Draw a bounding box around every malaria parasite.
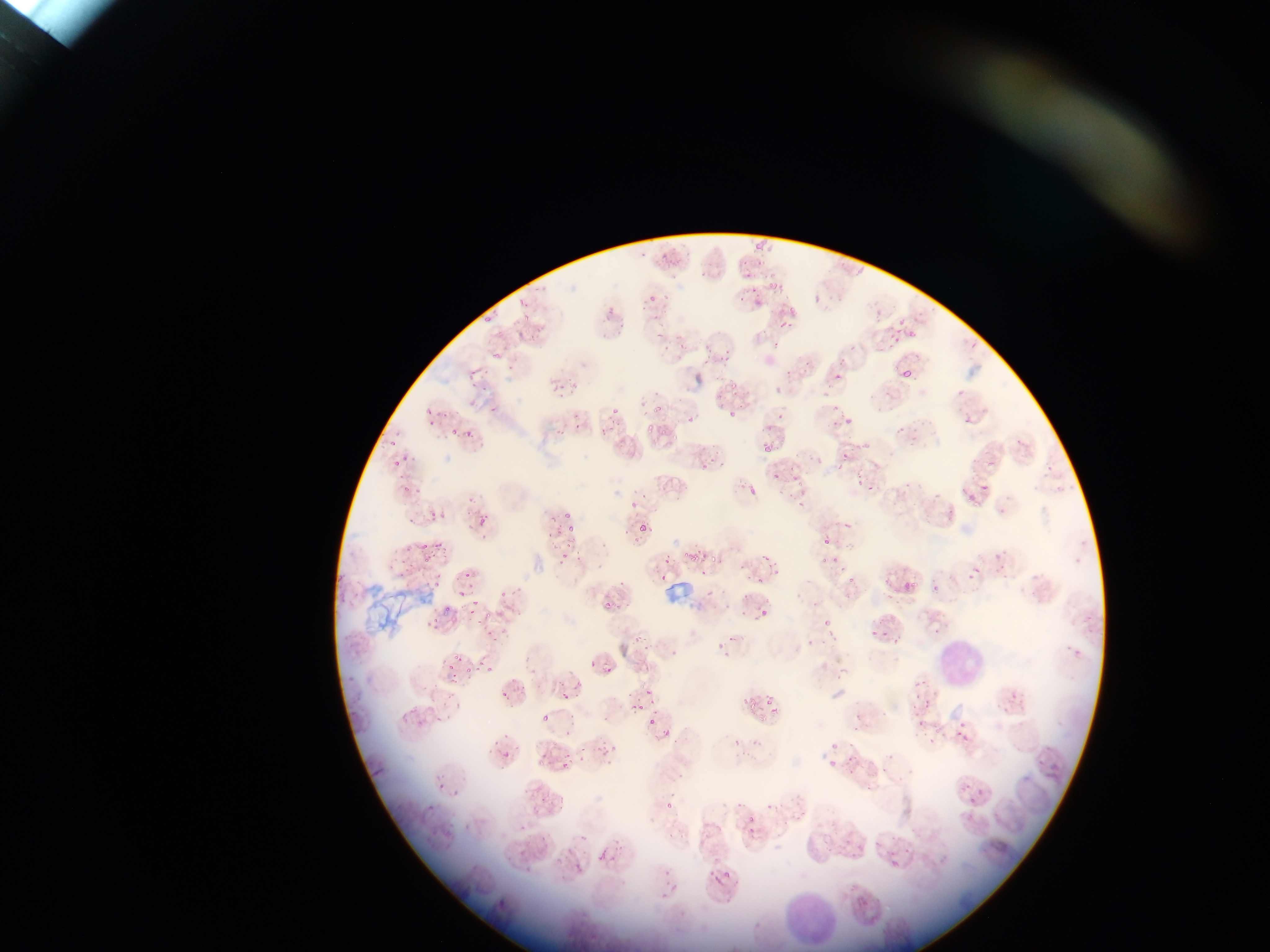
Approximate bounding boxes as (left, top, right, bottom) in pixels.
Malaria parasites: (766, 282, 774, 291), (605, 307, 616, 320), (536, 324, 545, 333), (904, 368, 913, 377), (957, 389, 965, 397), (603, 401, 619, 428), (649, 402, 660, 415), (488, 404, 501, 413), (830, 407, 855, 430), (728, 410, 737, 418), (683, 414, 703, 427), (426, 416, 438, 426), (643, 424, 657, 433), (594, 426, 608, 436), (464, 427, 474, 438), (569, 427, 579, 437), (451, 428, 460, 437), (661, 429, 667, 438), (673, 434, 684, 443), (760, 442, 775, 453), (834, 450, 850, 470), (788, 459, 807, 479), (391, 461, 401, 467), (696, 464, 712, 475), (771, 473, 786, 486), (850, 475, 867, 496), (398, 480, 418, 497), (746, 483, 768, 497), (959, 491, 978, 506), (783, 492, 799, 505), (627, 503, 643, 514), (407, 510, 417, 528), (428, 510, 440, 523), (561, 510, 569, 520), (476, 516, 489, 523), (565, 520, 579, 532), (637, 526, 647, 534), (824, 538, 832, 547), (419, 539, 432, 553), (435, 545, 455, 562), (555, 549, 568, 560), (661, 552, 673, 576), (683, 552, 700, 563), (708, 552, 718, 565), (815, 552, 834, 563), (761, 553, 777, 566), (421, 555, 430, 565), (827, 555, 841, 573), (396, 560, 413, 582), (963, 566, 985, 583), (695, 569, 708, 582), (653, 571, 666, 583), (459, 572, 478, 587), (754, 574, 769, 589), (843, 574, 861, 591), (431, 578, 444, 589), (905, 581, 917, 591), (932, 585, 940, 593), (806, 586, 833, 612), (457, 587, 468, 599), (608, 594, 633, 609), (600, 600, 613, 612), (758, 602, 773, 618), (466, 605, 481, 620), (442, 607, 455, 615), (821, 611, 841, 633), (422, 619, 445, 639), (876, 629, 886, 638), (799, 630, 823, 654), (627, 635, 638, 646), (712, 642, 727, 655), (447, 652, 465, 661), (588, 658, 598, 667), (445, 661, 459, 673), (603, 665, 615, 675), (463, 667, 468, 675), (481, 667, 492, 673), (446, 672, 463, 687), (636, 679, 653, 696), (575, 680, 584, 689), (557, 689, 573, 700), (500, 691, 508, 700), (911, 694, 936, 730), (742, 698, 753, 713), (765, 698, 770, 708), (632, 703, 641, 712), (411, 705, 424, 720), (434, 711, 454, 724), (645, 712, 656, 727), (542, 714, 550, 723), (946, 717, 973, 743), (411, 721, 428, 731), (559, 726, 574, 741), (917, 728, 948, 749), (660, 729, 670, 739), (728, 730, 757, 757), (487, 735, 504, 747), (827, 735, 844, 753), (575, 742, 587, 767), (596, 746, 618, 763), (502, 751, 511, 760), (821, 755, 839, 773), (839, 756, 863, 780), (555, 758, 572, 779), (868, 760, 894, 778), (435, 782, 445, 793), (454, 788, 462, 801), (965, 794, 982, 809), (552, 797, 565, 815), (665, 797, 673, 810), (424, 801, 435, 811), (531, 801, 544, 814), (747, 814, 753, 822), (463, 817, 481, 832), (510, 819, 522, 831), (661, 829, 676, 843), (538, 836, 547, 849), (513, 848, 524, 858), (597, 852, 606, 862), (574, 863, 583, 872), (660, 866, 672, 883), (723, 866, 733, 879), (708, 871, 723, 889), (659, 892, 668, 902) | approximate (x, y) pixel centers of objects too small to bound: (391, 441), (407, 550), (478, 662).

Summary:
  - Leukocyte locations: (936, 645, 984, 683), (785, 886, 835, 944)
  - Field of view: single
  - Country: Ghana
  - Capture: mobile-phone photograph through a microscope
  - Preparation: thin blood film
  - Image size: 1270×952 pixels